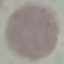
{
  "malaria_status": "uninfected",
  "preparation": "thin smear",
  "image_type": "cell patch, automatically extracted from a larger field of view and resized to 64 × 64 pixels",
  "stain": "Giemsa",
  "capture": "smartphone through the microscope eyepiece"
}